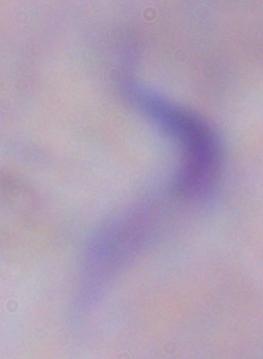
Summary:
  - Identification: trypanosome
  - Magnification: 1000x
  - Modality: micrograph